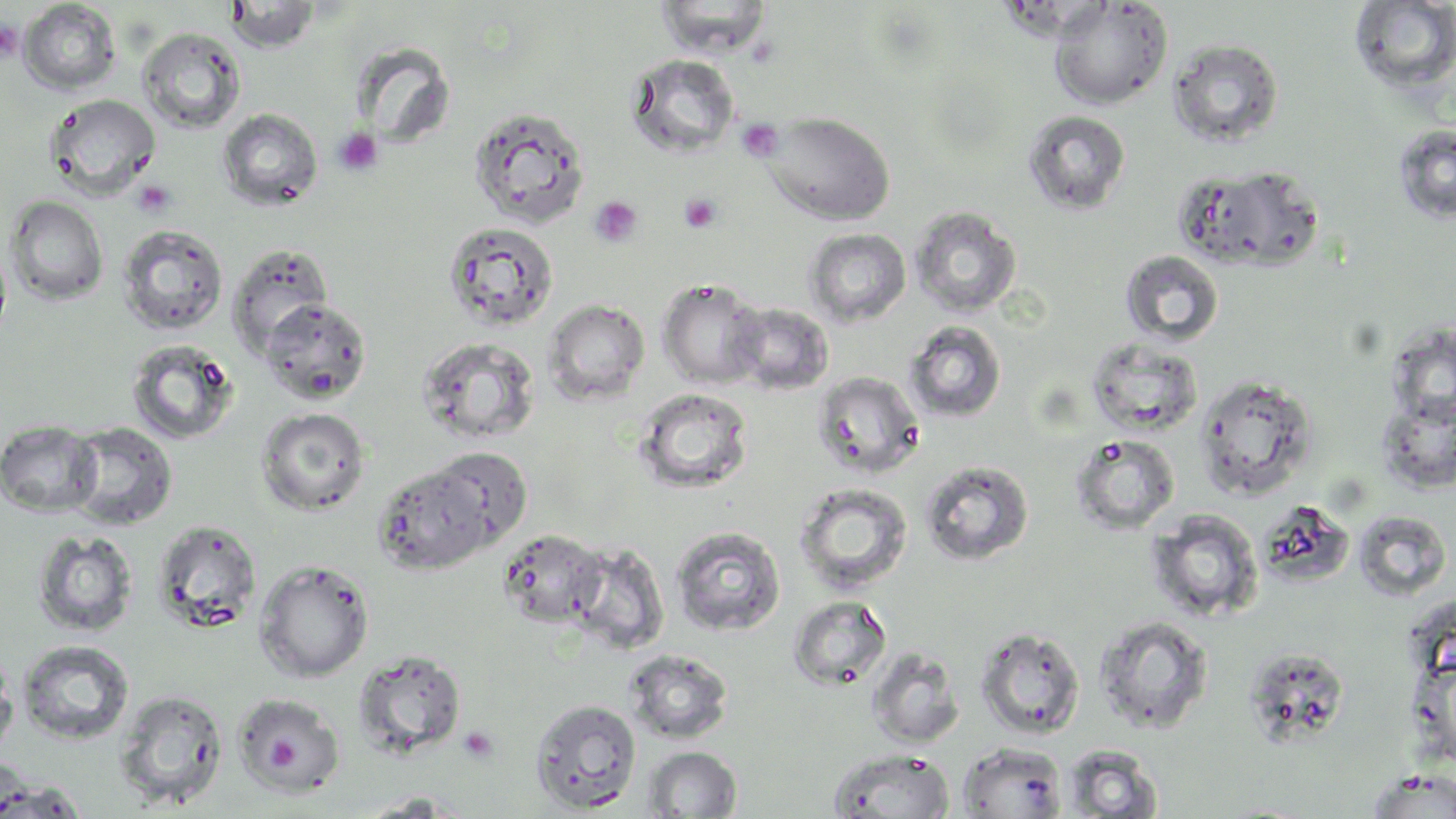
slide-level diagnosis = negative for blood parasites
platelet locations = approximate bounding boxes as (x1, y1, x2, y2) in pixels: (0, 21, 22, 61), (737, 118, 784, 163), (332, 128, 383, 176), (132, 180, 177, 218), (679, 193, 722, 234), (590, 196, 643, 249), (257, 722, 311, 776), (458, 726, 501, 765)
field of view = one of a larger specimen
stain = May-Grünwald-Giemsa
preparation = thin blood film
image size = 1456×819 pixels
magnification = 1000x
uninfected red blood cell locations = approximate bounding boxes as (x1, y1, x2, y2) in pixels: (655, 0, 773, 57), (18, 1, 121, 95), (224, 1, 322, 53), (1048, 1, 1172, 110), (1348, 1, 1456, 96), (138, 27, 246, 134), (1168, 38, 1284, 148), (350, 40, 456, 149), (625, 54, 740, 158), (44, 94, 161, 199), (468, 105, 590, 227), (217, 108, 323, 212), (1024, 110, 1131, 215), (765, 112, 895, 225), (1393, 124, 1456, 225), (1185, 165, 1326, 272), (5, 195, 109, 305), (909, 206, 1022, 318), (442, 220, 560, 332), (117, 224, 228, 335), (805, 228, 912, 326), (0, 240, 13, 351), (228, 243, 334, 356), (1120, 250, 1225, 347), (657, 278, 767, 389), (260, 298, 373, 405), (543, 299, 650, 405), (729, 302, 835, 395), (904, 321, 1007, 423), (1386, 324, 1456, 430), (417, 337, 541, 446), (1085, 338, 1204, 437), (125, 339, 239, 446), (812, 370, 925, 479), (1195, 374, 1319, 501), (632, 387, 754, 495), (1377, 395, 1456, 494), (256, 407, 371, 515), (1, 420, 102, 517), (65, 421, 179, 531), (1070, 433, 1180, 535), (431, 447, 533, 547), (919, 459, 1034, 566), (372, 464, 493, 575), (794, 482, 914, 596), (1251, 499, 1358, 588), (1147, 510, 1264, 622), (1354, 510, 1453, 601), (152, 520, 262, 631), (670, 526, 786, 637), (497, 528, 608, 627), (32, 530, 139, 637), (567, 542, 670, 654), (254, 559, 374, 682), (788, 595, 892, 691), (1093, 615, 1214, 735), (974, 626, 1086, 739), (17, 639, 135, 745), (867, 647, 965, 749), (1244, 647, 1351, 747), (0, 648, 18, 765), (624, 648, 734, 744), (353, 649, 467, 758), (114, 689, 229, 810), (233, 691, 347, 795), (530, 698, 642, 813), (958, 742, 1068, 818), (1061, 744, 1164, 818), (642, 746, 742, 818), (828, 748, 954, 819), (0, 757, 33, 819), (1364, 769, 1456, 818), (0, 779, 89, 818), (354, 791, 470, 817)
modality = light microscopy